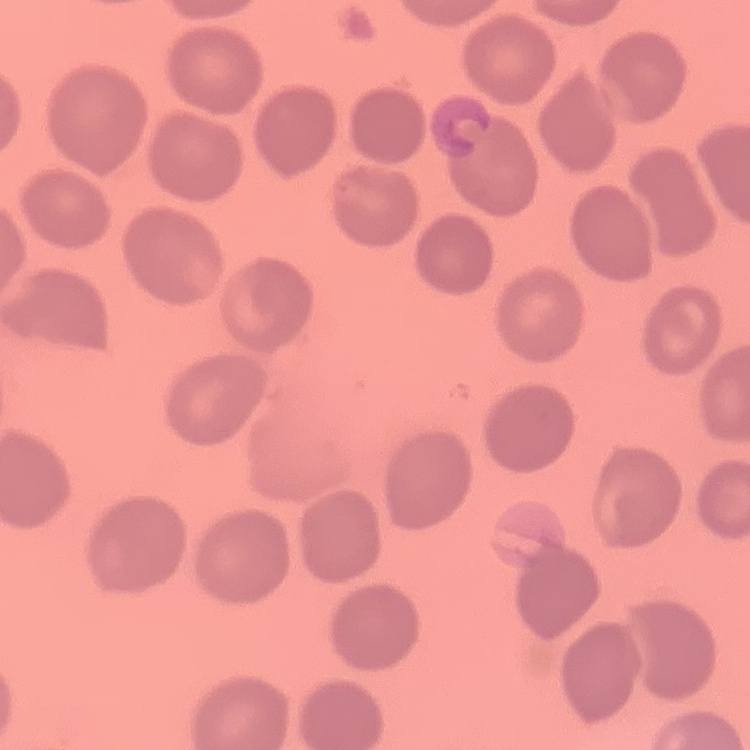
red blood cell morphology = no rouleaux formation
image type = square crop of a larger photomicrograph
stain = Field's or Giemsa
preparation = thin blood smear